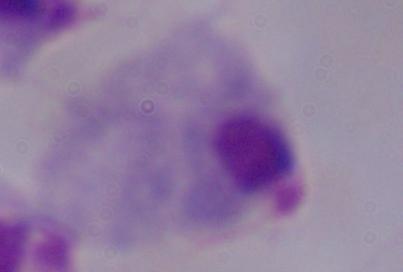 Photomicrograph. Captured at 1000x magnification. A trichomonad is shown.